Locate every blood parasite and identify its species.
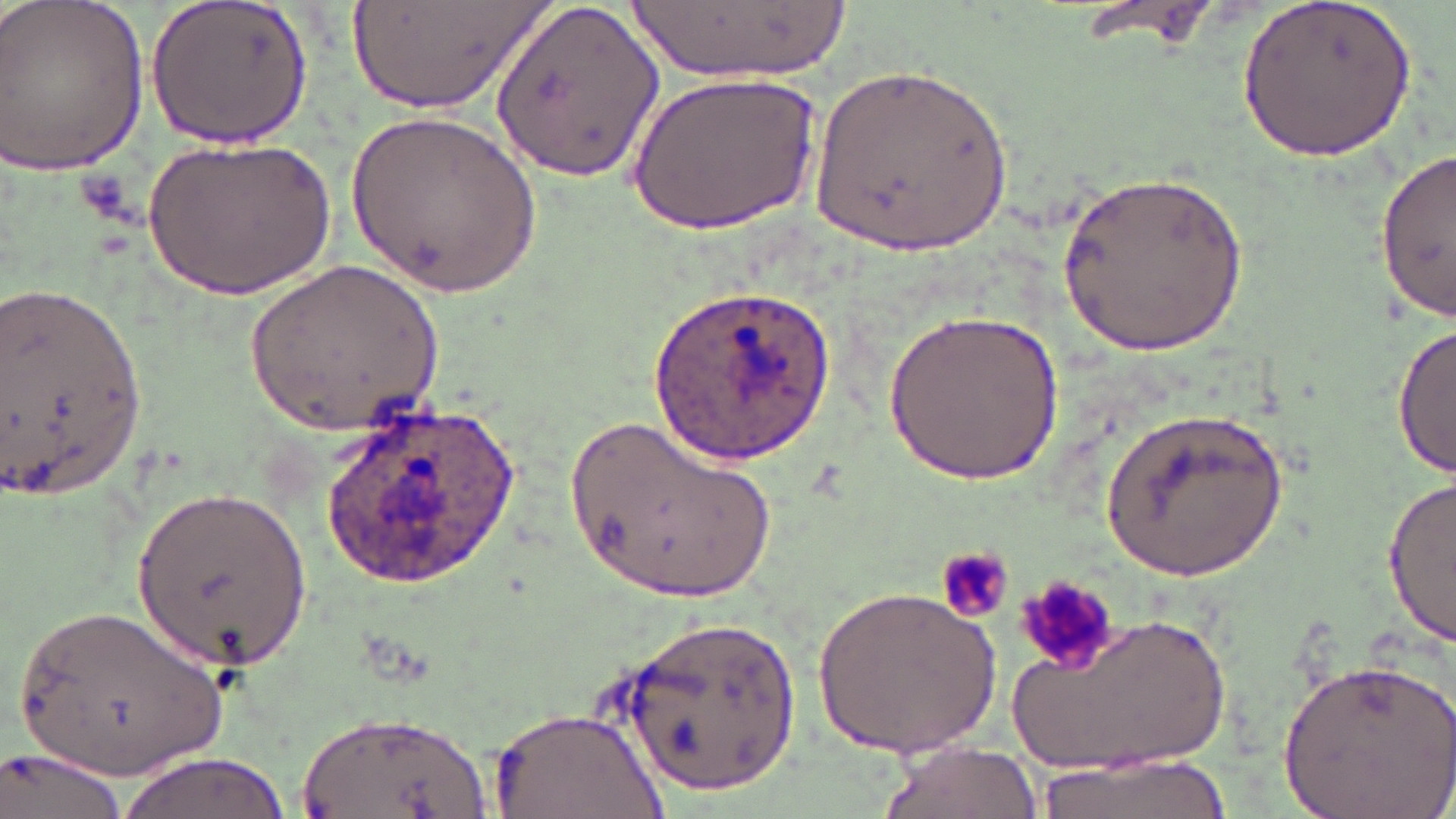

Approximate bounding boxes as (x1, y1, x2, y2) in pixels.
Plasmodium ovale-infected red blood cells: (655, 282, 837, 463), (313, 402, 531, 594).
No Plasmodium falciparum, Plasmodium malariae, Plasmodium vivax, Babesia divergens, or Trypanosoma brucei observed.

slide-level diagnosis = Plasmodium ovale
uninfected red blood cell locations = approximate bounding boxes as (x1, y1, x2, y2) in pixels: (145, 0, 313, 150), (349, 0, 550, 114), (1069, 0, 1225, 50), (491, 2, 660, 184), (627, 2, 851, 84), (0, 3, 154, 180), (1236, 3, 1417, 163), (804, 62, 1016, 259), (631, 67, 821, 236), (349, 106, 538, 302), (147, 132, 332, 301), (1376, 149, 1453, 320), (1056, 173, 1248, 358), (246, 258, 442, 442), (1, 276, 151, 501), (887, 310, 1066, 483), (1392, 323, 1454, 479), (1095, 400, 1290, 585), (567, 409, 779, 608), (1381, 476, 1456, 645), (135, 481, 310, 670), (939, 544, 1015, 620), (817, 584, 1003, 758), (11, 600, 236, 780), (1000, 609, 1241, 782), (621, 613, 801, 791), (1277, 655, 1455, 818), (493, 706, 667, 819), (296, 709, 494, 819), (875, 738, 1040, 819), (2, 747, 129, 819), (117, 751, 296, 819), (1035, 751, 1229, 819)
preparation = thin blood film
field of view = one of a larger specimen
platelet locations = approximate bounding boxes as (x1, y1, x2, y2) in pixels: (936, 542, 1017, 622), (1012, 573, 1124, 672)
modality = light microscopy
magnification = 1000x
image size = 1456×819 pixels
stain = May-Grünwald-Giemsa